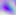

Photomicrograph. Toxoplasma gondii is seen. Captured at 400x magnification.